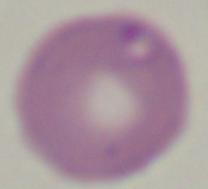

{
  "identification": "Babesia",
  "magnification": "1000x",
  "modality": "photomicrograph"
}